Describe the morphology of the red blood cells.
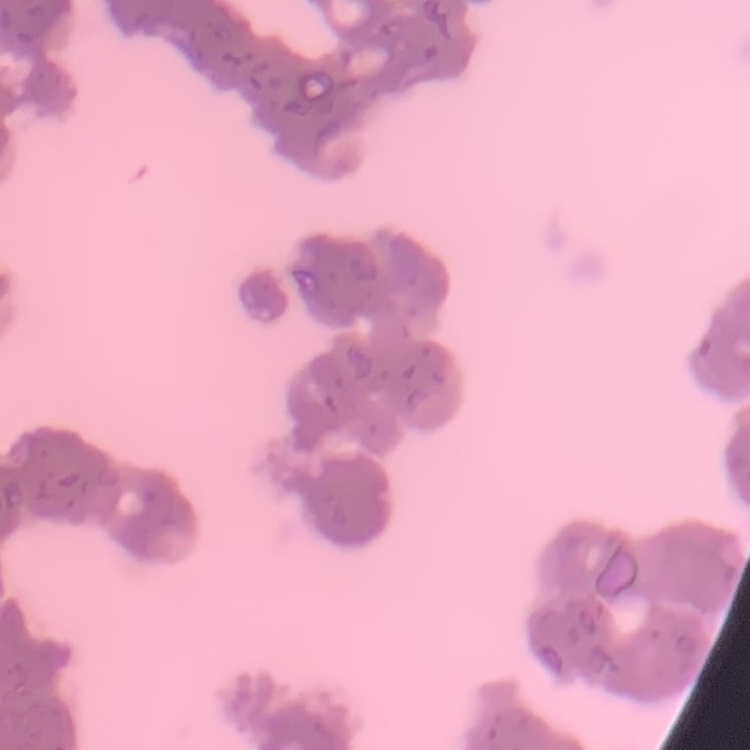
They show rouleaux formation.

preparation = thin peripheral smear
stain = Field's or Giemsa
image type = square crop of a larger photomicrograph